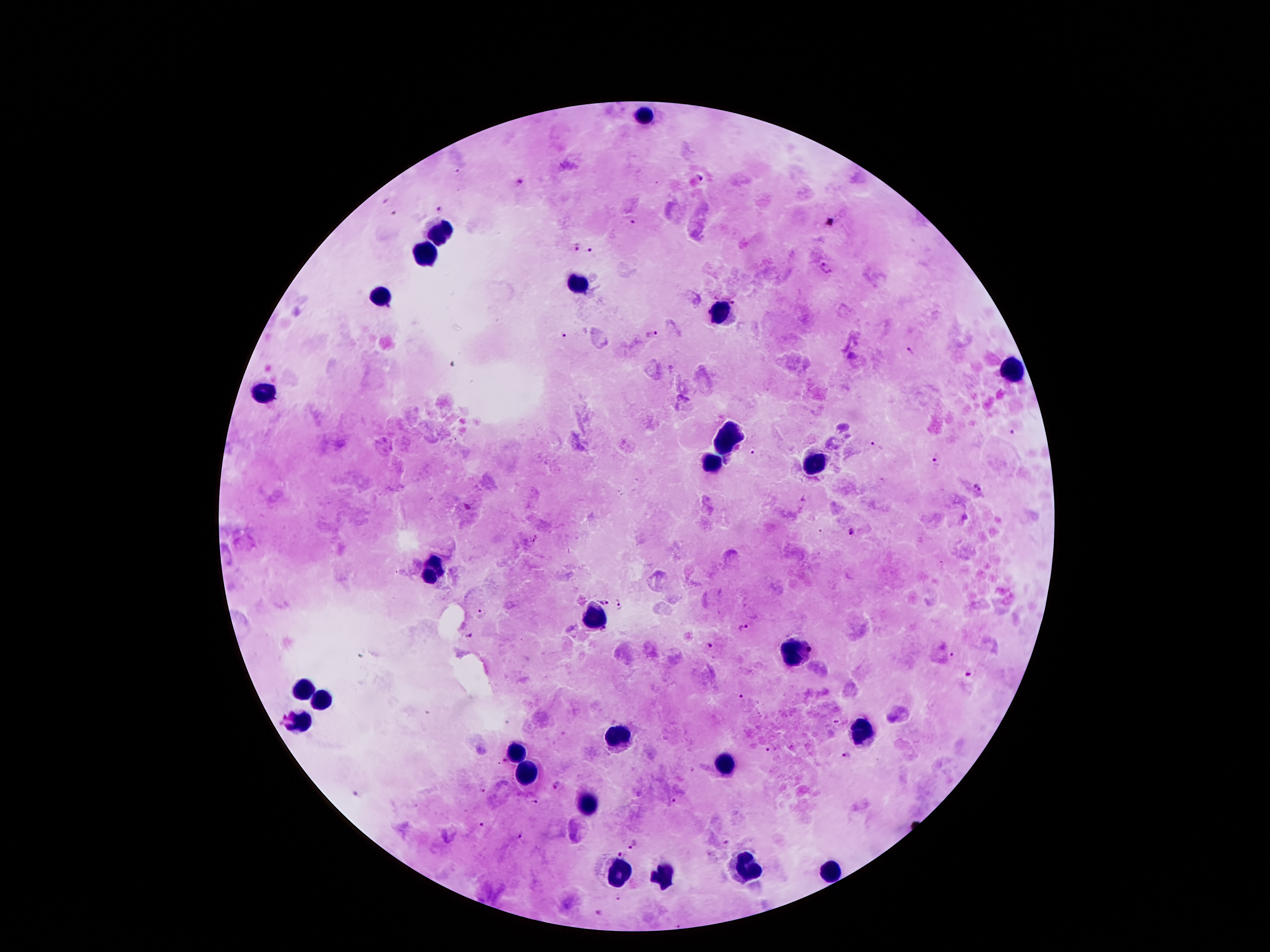
capture: smartphone through the microscope eyepiece
leukocyte_locations: 'approximate object centers, in pixels from the top-left corner: (x=641, y=116), (x=439, y=234), (x=423, y=256), (x=577, y=284), (x=379, y=298), (x=723, y=312), (x=1013, y=368), (x=263, y=394), (x=727, y=434), (x=815, y=460), (x=711, y=464), (x=435, y=562), (x=431, y=576), (x=595, y=616), (x=793, y=652), (x=303, y=692), (x=321, y=702), (x=299, y=720), (x=863, y=730), (x=619, y=738), (x=513, y=754), (x=725, y=764), (x=525, y=774), (x=585, y=806), (x=747, y=872), (x=829, y=872), (x=617, y=874), (x=663, y=880)'
image_size: 1270×952 pixels
stain: Giemsa
patient_malaria_status: infected with Plasmodium falciparum
magnification: 100x
plasmodium_parasite_locations: 'approximate object centers, in pixels from the top-left corner: (x=702, y=179), (x=519, y=181), (x=387, y=198), (x=438, y=209), (x=394, y=212), (x=631, y=219), (x=577, y=245), (x=591, y=250), (x=565, y=331), (x=649, y=336), (x=911, y=351), (x=1013, y=433), (x=875, y=445), (x=754, y=451), (x=934, y=463), (x=977, y=489), (x=466, y=504), (x=852, y=530), (x=619, y=599), (x=605, y=603), (x=481, y=614), (x=743, y=626), (x=471, y=637), (x=707, y=644), (x=952, y=654), (x=969, y=673), (x=740, y=695), (x=837, y=721), (x=768, y=747), (x=847, y=756), (x=558, y=784), (x=483, y=790), (x=356, y=792), (x=674, y=800), (x=530, y=802), (x=483, y=823), (x=519, y=835), (x=634, y=843), (x=624, y=854), (x=601, y=912)'
field_of_view: one from this slide
preparation: thick blood film